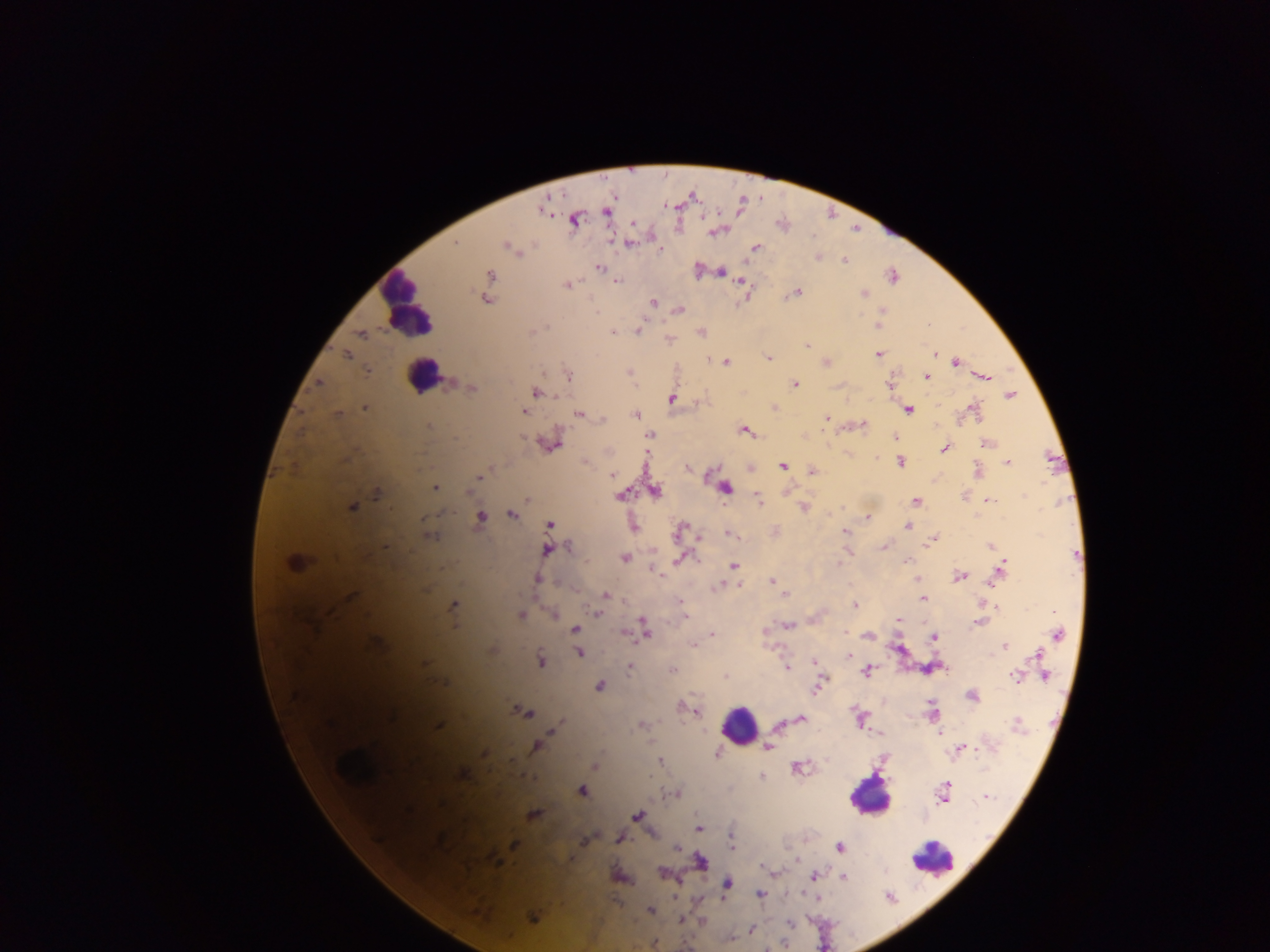
Approximate centers as [x, y] in pixels.
Summary:
  - Malaria parasite locations: [545, 207], [608, 210], [573, 219], [716, 230], [629, 242], [456, 244], [506, 246], [755, 248], [661, 249], [818, 257], [844, 260], [599, 266], [698, 270], [720, 271], [489, 275], [892, 275], [616, 281], [742, 281], [566, 285], [795, 292], [863, 293], [746, 295], [486, 299], [652, 302], [679, 309], [881, 317], [878, 324], [639, 329], [613, 331], [700, 332], [361, 333], [669, 340], [807, 344], [934, 353], [346, 354], [878, 354], [766, 358], [710, 360], [825, 361], [955, 361], [724, 362], [366, 370], [629, 373], [568, 376], [925, 376], [982, 376], [318, 383], [450, 384], [795, 384], [889, 384], [472, 387], [534, 392], [1009, 396], [672, 398], [773, 406], [365, 407], [907, 409], [973, 410], [524, 411], [337, 414], [578, 414], [635, 414], [600, 417], [826, 418], [861, 425], [429, 426], [745, 430], [649, 434], [895, 438], [550, 442], [986, 444], [945, 447], [900, 461], [585, 462], [1006, 462], [782, 465], [688, 467], [750, 467], [812, 471], [977, 471], [611, 475], [479, 476], [435, 488], [725, 488], [787, 490], [654, 491], [377, 492], [620, 494], [965, 495], [527, 498], [758, 499], [987, 500], [916, 502], [351, 506], [804, 507], [512, 513], [479, 517], [867, 517], [910, 522], [550, 525], [633, 525], [908, 526], [680, 530], [845, 531], [729, 533], [428, 536], [698, 537], [932, 539], [990, 546], [884, 547], [546, 549], [846, 551], [624, 557], [680, 557], [906, 560], [294, 563], [733, 565], [656, 570], [1000, 570], [959, 575], [537, 578], [915, 579], [773, 581], [738, 583], [718, 586], [785, 594], [604, 595], [350, 597], [923, 598], [680, 601], [982, 603], [453, 605], [854, 605], [994, 606], [553, 613], [599, 613], [519, 615], [684, 615], [899, 620], [979, 621], [787, 625], [643, 629], [575, 630], [623, 633], [712, 634], [868, 634], [1057, 634], [933, 636], [375, 643], [693, 645], [1003, 645], [491, 650], [579, 652], [1039, 653], [848, 655], [540, 659], [814, 662], [423, 664], [630, 667], [787, 667], [673, 670], [867, 670], [725, 676], [1017, 676], [1044, 676], [822, 680], [443, 683], [818, 684], [599, 685], [972, 695], [680, 707], [693, 709], [521, 710], [932, 714], [859, 718], [800, 719], [1017, 724], [437, 725], [641, 725], [779, 725], [556, 728], [940, 732], [880, 735], [536, 746], [767, 747], [959, 749], [485, 753], [717, 753], [660, 760], [594, 765], [798, 767], [462, 773], [761, 776], [581, 790], [944, 792], [676, 794], [987, 797], [533, 815], [636, 817], [698, 828], [619, 838], [585, 839], [438, 840], [731, 843], [514, 844], [677, 847], [839, 847], [494, 859], [699, 862], [662, 873], [772, 873], [618, 876], [813, 876], [844, 877], [725, 885], [758, 893], [650, 910], [533, 916], [700, 919], [680, 920], [751, 930], [729, 939], [653, 943]
  - Leukocyte locations: [407, 307], [421, 375], [739, 725], [869, 795], [931, 859]
  - Preparation: thick blood smear
  - Capture: mobile-phone photograph through a microscope
  - Image size: 1270×952 pixels
  - Field of view: single
  - Country: Ghana